Give the extent of all Plasmodium falciparum-infected red blood cells.
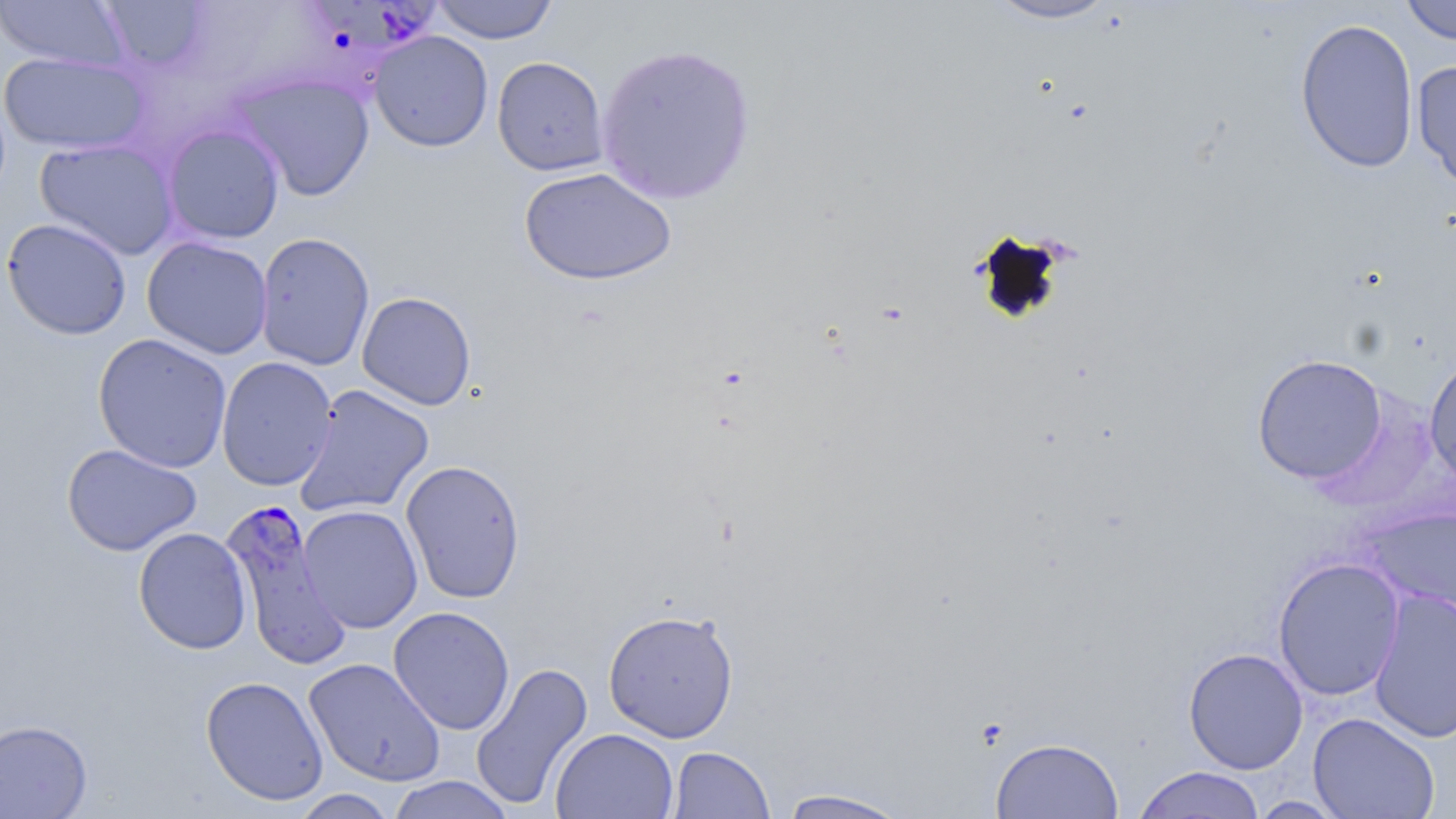

Approximate bounding boxes as named x1/y1/x2/y2 corners in pixels.
Plasmodium falciparum-infected red blood cells: (x1=308, y1=3, x2=440, y2=53), (x1=219, y1=499, x2=349, y2=665).

slide-level diagnosis = Plasmodium falciparum
magnification = 1000x
stain = May-Grünwald-Giemsa
field of view = one of a larger specimen
modality = light microscopy
image size = 1456×819 pixels
preparation = thin blood smear
uninfected red blood cell locations = approximate bounding boxes as named x1/y1/x2/y2 corners in pixels: (x1=0, y1=0, x2=129, y2=71), (x1=99, y1=0, x2=212, y2=74), (x1=431, y1=0, x2=559, y2=44), (x1=983, y1=0, x2=1124, y2=26), (x1=1400, y1=0, x2=1456, y2=46), (x1=1295, y1=17, x2=1419, y2=174), (x1=369, y1=31, x2=494, y2=152), (x1=595, y1=42, x2=757, y2=205), (x1=0, y1=52, x2=151, y2=155), (x1=492, y1=56, x2=609, y2=176), (x1=1411, y1=59, x2=1456, y2=193), (x1=228, y1=71, x2=375, y2=202), (x1=162, y1=124, x2=285, y2=244), (x1=34, y1=138, x2=179, y2=260), (x1=519, y1=166, x2=676, y2=286), (x1=1, y1=218, x2=132, y2=340), (x1=254, y1=232, x2=375, y2=372), (x1=142, y1=236, x2=273, y2=359), (x1=357, y1=291, x2=477, y2=410), (x1=92, y1=333, x2=232, y2=473), (x1=1423, y1=352, x2=1456, y2=492), (x1=1251, y1=354, x2=1388, y2=485), (x1=216, y1=356, x2=338, y2=491), (x1=293, y1=384, x2=435, y2=519), (x1=62, y1=443, x2=201, y2=556), (x1=401, y1=459, x2=526, y2=604), (x1=297, y1=504, x2=423, y2=633), (x1=1360, y1=506, x2=1455, y2=619), (x1=133, y1=527, x2=252, y2=654), (x1=1272, y1=556, x2=1405, y2=701), (x1=1368, y1=588, x2=1456, y2=744), (x1=388, y1=606, x2=515, y2=734), (x1=603, y1=608, x2=739, y2=742), (x1=1183, y1=647, x2=1309, y2=774), (x1=304, y1=657, x2=446, y2=787), (x1=469, y1=661, x2=594, y2=811), (x1=201, y1=675, x2=329, y2=805), (x1=1308, y1=712, x2=1440, y2=818), (x1=0, y1=719, x2=92, y2=819), (x1=550, y1=728, x2=679, y2=819), (x1=990, y1=737, x2=1124, y2=819), (x1=668, y1=746, x2=775, y2=818), (x1=1133, y1=766, x2=1266, y2=818), (x1=386, y1=775, x2=516, y2=819), (x1=777, y1=788, x2=913, y2=818), (x1=289, y1=789, x2=400, y2=818), (x1=1249, y1=796, x2=1349, y2=818)